Identify the preparation type.
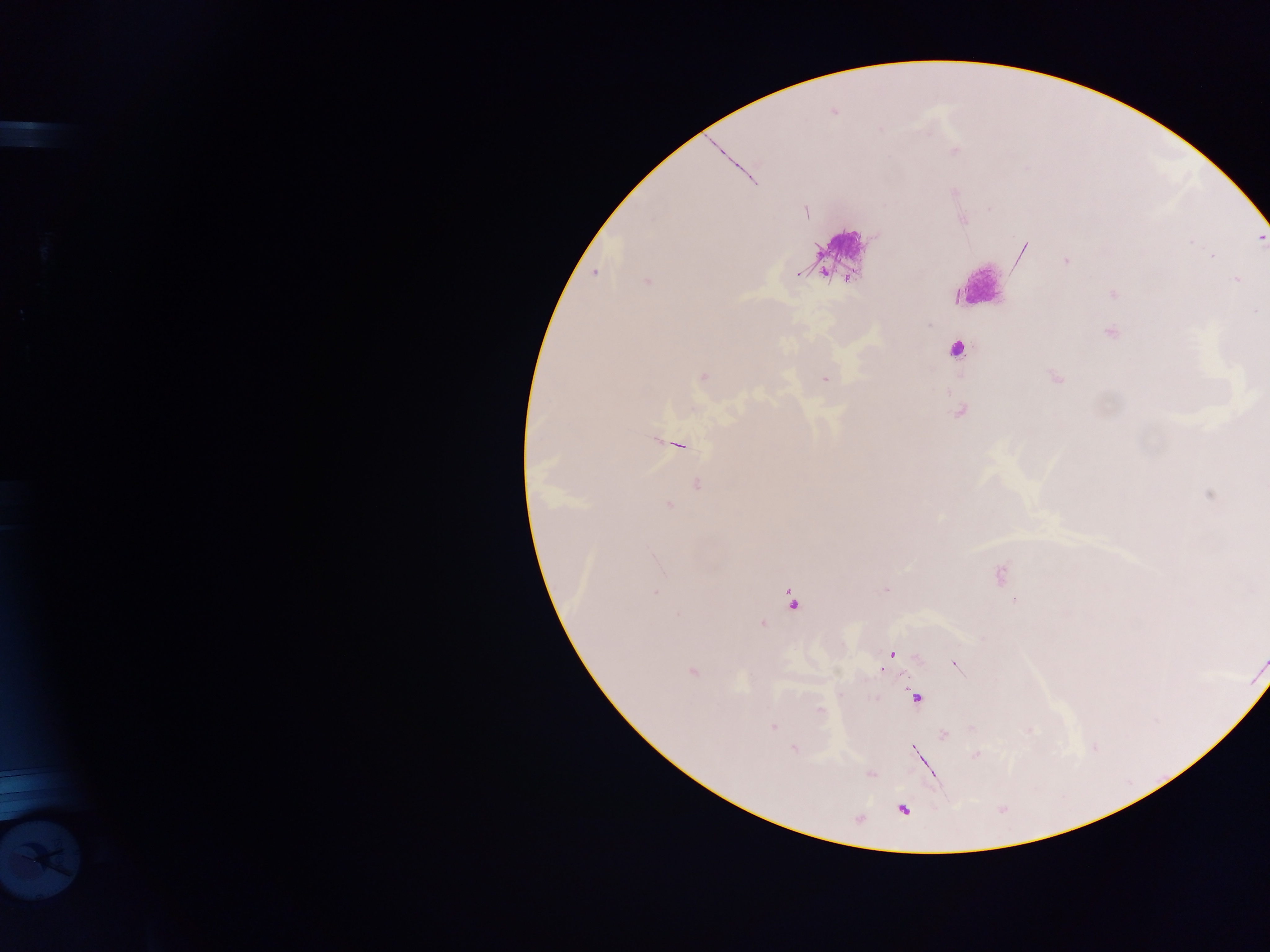
Thick blood smear.

Approximate centers as x y in pixels. Plasmodium parasite locations: 955 151; 806 212; 1066 261; 595 273; 1236 279; 646 281; 1113 294; 1256 310; 703 376; 824 379; 697 484; 669 506; 1000 575; 886 590; 655 593; 793 600; 1015 600; 763 625; 891 654; 956 666; 692 672; 916 697; 821 710; 774 727; 944 735; 793 748; 914 749; 977 755; 903 809. Leukocyte locations: 843 247; 978 280; 956 350. Mobile-phone photograph taken through the microscope. One field of view. Image is 1270×952 pixels. Collected in Ghana.